Outline each white blood cell.
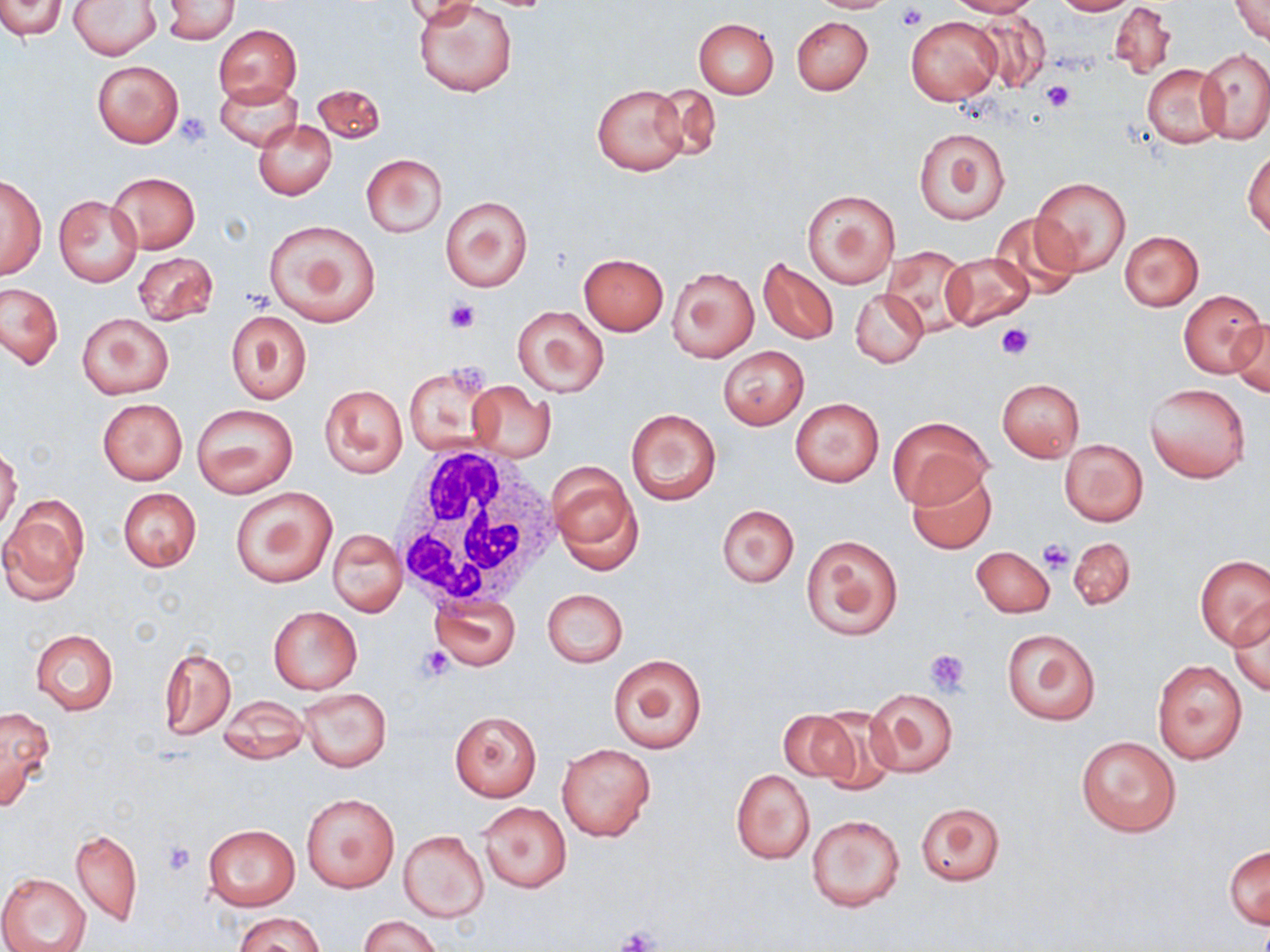

Approximate bounding boxes as [x1, y1, x2, y2] in pixels.
White blood cells: [390, 444, 566, 610].

Platelet locations: [897, 4, 926, 30], [1042, 81, 1076, 112], [178, 112, 211, 147], [445, 296, 480, 334], [996, 324, 1033, 359], [447, 362, 492, 395], [1038, 540, 1074, 573], [419, 646, 454, 681], [924, 647, 971, 695], [161, 840, 196, 876], [615, 928, 660, 952]. Uninfected red blood cell locations: [0, 0, 65, 39], [806, 0, 900, 13], [946, 0, 1039, 17], [1052, 0, 1136, 16], [1231, 0, 1269, 45], [71, 1, 160, 58], [162, 1, 239, 43], [403, 1, 481, 29], [414, 1, 520, 97], [1108, 1, 1176, 80], [973, 12, 1051, 92], [791, 16, 873, 96], [907, 16, 1002, 105], [692, 18, 778, 98], [213, 24, 300, 107], [1198, 48, 1270, 144], [91, 60, 184, 147], [1142, 64, 1229, 147], [215, 80, 302, 151], [313, 82, 385, 146], [590, 83, 691, 176], [649, 84, 721, 161], [254, 119, 336, 199], [913, 126, 1010, 224], [1245, 149, 1270, 238], [360, 154, 447, 237], [107, 172, 200, 253], [1030, 175, 1131, 277], [0, 177, 46, 279], [800, 189, 901, 289], [438, 194, 534, 292], [53, 195, 143, 286], [989, 212, 1081, 296], [263, 219, 383, 325], [1119, 231, 1203, 310], [879, 245, 975, 335], [132, 251, 218, 324], [939, 251, 1033, 330], [577, 253, 669, 334], [758, 257, 838, 344], [667, 266, 759, 362], [1, 284, 63, 368], [850, 288, 927, 367], [1177, 290, 1266, 378], [513, 306, 609, 397], [225, 310, 312, 404], [76, 312, 173, 400], [1231, 318, 1270, 396], [718, 345, 810, 430], [404, 363, 497, 456], [996, 378, 1085, 461], [466, 382, 556, 462], [1144, 382, 1251, 484], [320, 384, 407, 478], [97, 399, 188, 485], [790, 399, 884, 486], [192, 404, 298, 498], [625, 407, 722, 505], [889, 414, 990, 508], [1059, 439, 1148, 526], [0, 448, 22, 533], [548, 460, 641, 570], [907, 469, 997, 554], [230, 486, 337, 588], [118, 488, 201, 571], [0, 499, 88, 603], [717, 504, 799, 587], [327, 528, 406, 615], [800, 534, 903, 641], [1067, 536, 1136, 610], [972, 547, 1054, 617], [1196, 556, 1270, 649], [542, 589, 627, 667], [429, 594, 520, 671], [1230, 604, 1270, 697], [269, 607, 361, 694], [1000, 627, 1101, 726], [31, 629, 118, 713], [160, 644, 236, 739], [609, 654, 708, 755], [1152, 660, 1248, 763], [299, 688, 391, 771], [866, 688, 959, 778], [216, 698, 311, 765], [0, 705, 55, 811], [814, 706, 899, 793], [777, 709, 858, 782], [449, 710, 542, 802], [1076, 735, 1182, 837], [557, 744, 655, 841], [730, 768, 815, 864], [302, 793, 399, 893], [477, 801, 571, 893], [915, 801, 1007, 885], [805, 813, 905, 913], [202, 824, 300, 912], [70, 828, 142, 926], [400, 831, 489, 922], [1225, 844, 1269, 929], [0, 873, 90, 952], [234, 913, 327, 952], [359, 915, 443, 952]. Slide-level diagnosis: no evidence of blood parasites. Thin blood smear. Optical microscopy. Image is 1270×952 pixels. Captured at 1000x magnification. One field of a larger specimen. May-Grünwald-Giemsa stain.